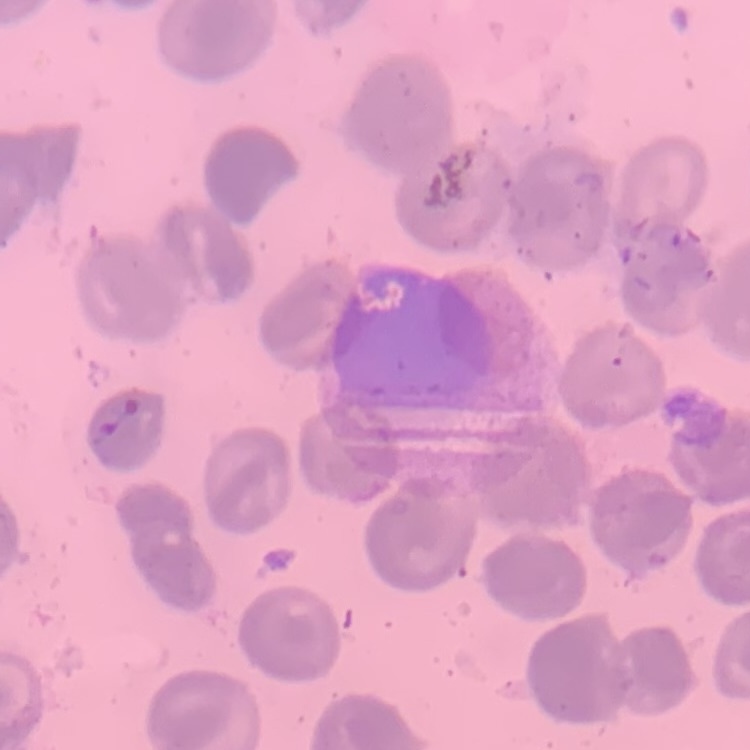 The red blood cells exhibit no rouleaux formation. Thin peripheral smear. Stained with either Field's or Giemsa. Square crop of a larger photomicrograph.